Name the parasite shown.
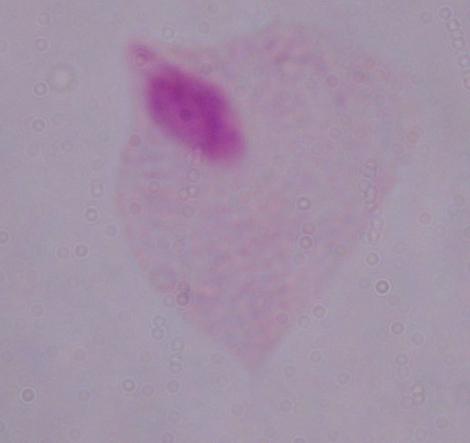

A trichomonad.

modality = photomicrograph
magnification = 1000x